Locate Plasmodium parasites and leukocytes.
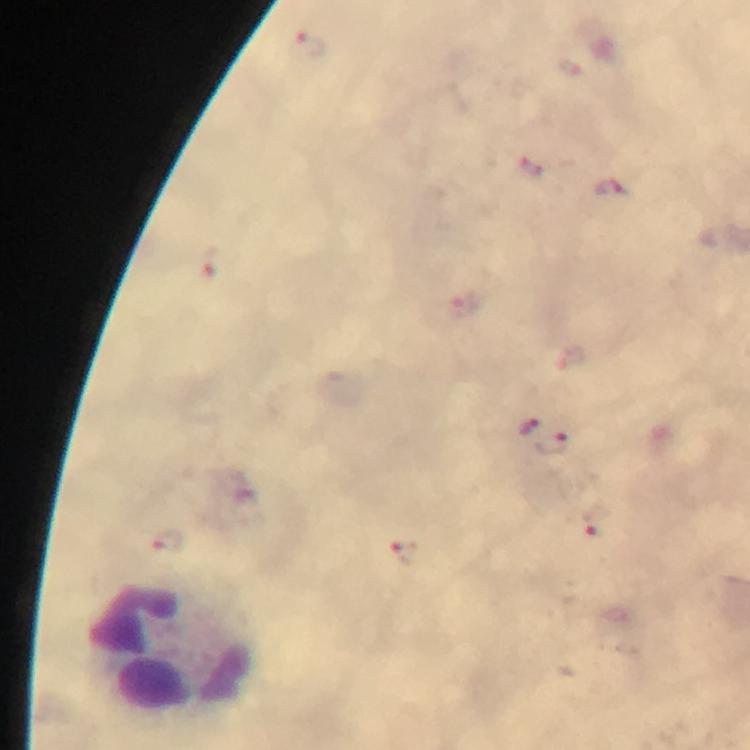

No Plasmodium parasites seen.
Approximate centers as (x, y) in pixels.
Leukocytes: (169, 652).

Summary:
  - Preparation: thick blood film
  - Cropped from: one field of view
  - Stain: Giemsa
  - Context: from a malaria diagnostic workup
  - Magnification: 100x
  - Image size: 750×750 pixels
  - Capture: smartphone camera through the microscope
  - Immersion oil: used